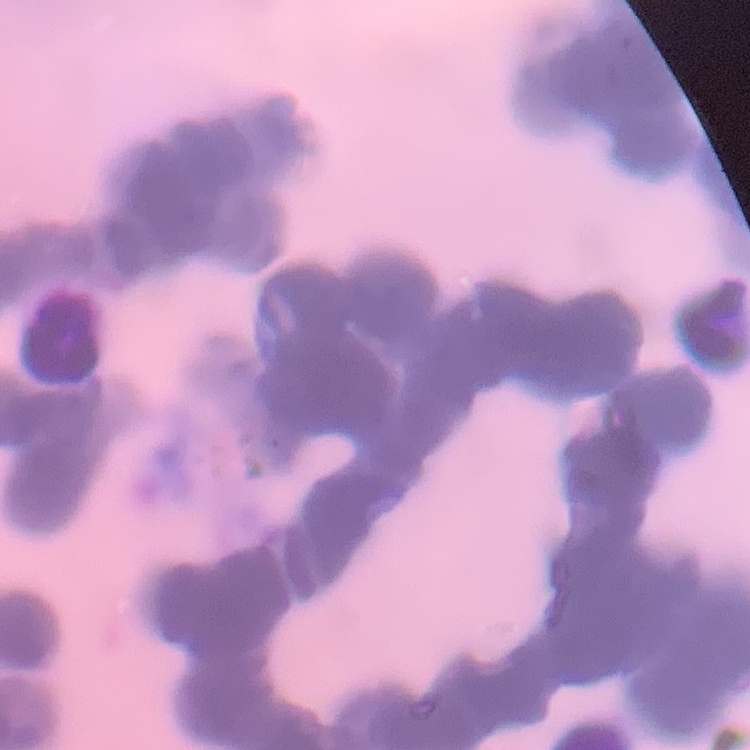
red blood cell morphology = rouleaux formation
stain = Field's or Giemsa
preparation = thin blood film
image type = square crop of a larger photomicrograph